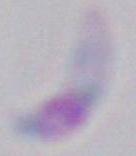
identification: Toxoplasma gondii
modality: photomicrograph
magnification: 1000x